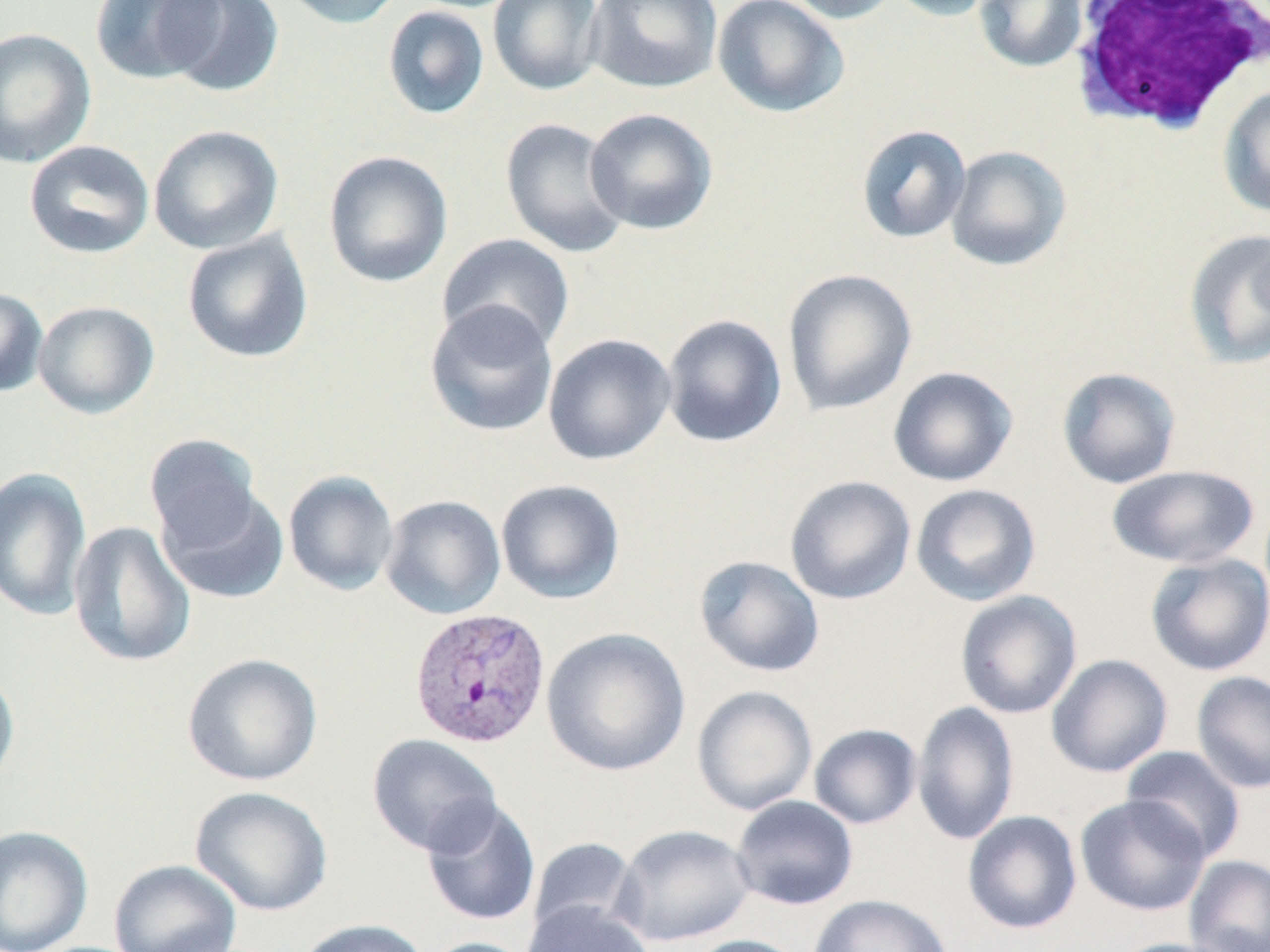

slide_level_diagnosis: Plasmodium vivax
uninfected_red_blood_cell_locations: 'approximate bounding boxes as (x1,y1)-(x2,y2) corner pairs in pixels: (90,0)-(223,85), (161,0)-(284,97), (277,0)-(406,30), (488,0)-(605,96), (585,0)-(723,93), (713,0)-(849,118), (777,0)-(900,24), (882,0)-(1003,21), (973,0)-(1089,73), (382,6)-(490,120), (0,27)-(96,169), (1218,85)-(1270,218), (584,108)-(718,235), (500,117)-(630,258), (148,124)-(284,254), (856,125)-(971,244), (24,140)-(155,259), (945,145)-(1071,271), (323,150)-(453,288), (1183,228)-(1270,370), (182,231)-(314,363), (437,233)-(575,354), (782,268)-(918,417), (0,287)-(48,397), (424,300)-(559,438), (34,301)-(159,419), (661,314)-(787,448), (543,333)-(676,466), (887,366)-(1018,487), (1057,367)-(1181,489), (145,434)-(262,550), (1106,464)-(1259,568), (0,468)-(92,620), (283,470)-(399,596), (785,475)-(916,605), (495,478)-(626,604), (910,484)-(1042,606), (157,485)-(289,604), (379,494)-(506,620), (68,520)-(196,668), (1145,553)-(1270,676), (694,555)-(825,677), (955,590)-(1083,719), (540,627)-(691,777), (182,653)-(323,787), (1045,654)-(1173,778), (0,668)-(20,793), (1191,671)-(1270,794), (692,684)-(817,816), (911,701)-(1019,845), (808,724)-(922,829), (366,733)-(503,857), (1121,745)-(1246,863), (189,786)-(333,917), (1075,794)-(1210,916), (730,795)-(859,910), (421,798)-(541,927), (962,810)-(1082,935), (612,824)-(756,947), (0,825)-(93,952), (527,837)-(640,939), (1184,855)-(1269,951), (108,859)-(242,952), (809,894)-(952,952), (521,900)-(655,952), (294,918)-(430,952), (683,935)-(808,952), (418,936)-(538,952), (1108,937)-(1236,952)'
stain: May-Grünwald-Giemsa
magnification: 1000x
image_size: 1270×952 pixels
modality: light microscopy
plasmodium_vivax_infected_red_blood_cell_locations: 'approximate bounding boxes as (x1,y1)-(x2,y2) corner pairs in pixels: (409,605)-(552,749)'
field_of_view: single
preparation: thin blood film
white_blood_cell_locations: 'approximate bounding boxes as (x1,y1)-(x2,y2) corner pairs in pixels: (1064,1)-(1270,136)'